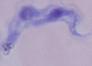

identification: trypanosome
modality: micrograph
magnification: 1000x